Report the malaria status of this cell.
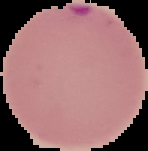
Parasitized.

Summary:
  - Preparation: thin blood smear
  - Image type: segmented cell region with the area outside set to black
  - Image size: 148×151 pixels